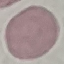 Malaria status: uninfected. Photographed with a smartphone camera at the microscope eyepiece. Automatically extracted cell patch, resized to 64 × 64 pixels. Thin blood film. Giemsa stain.